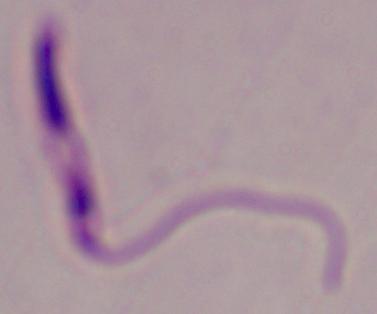
magnification = 1000x
modality = photomicrograph
identification = Leishmania